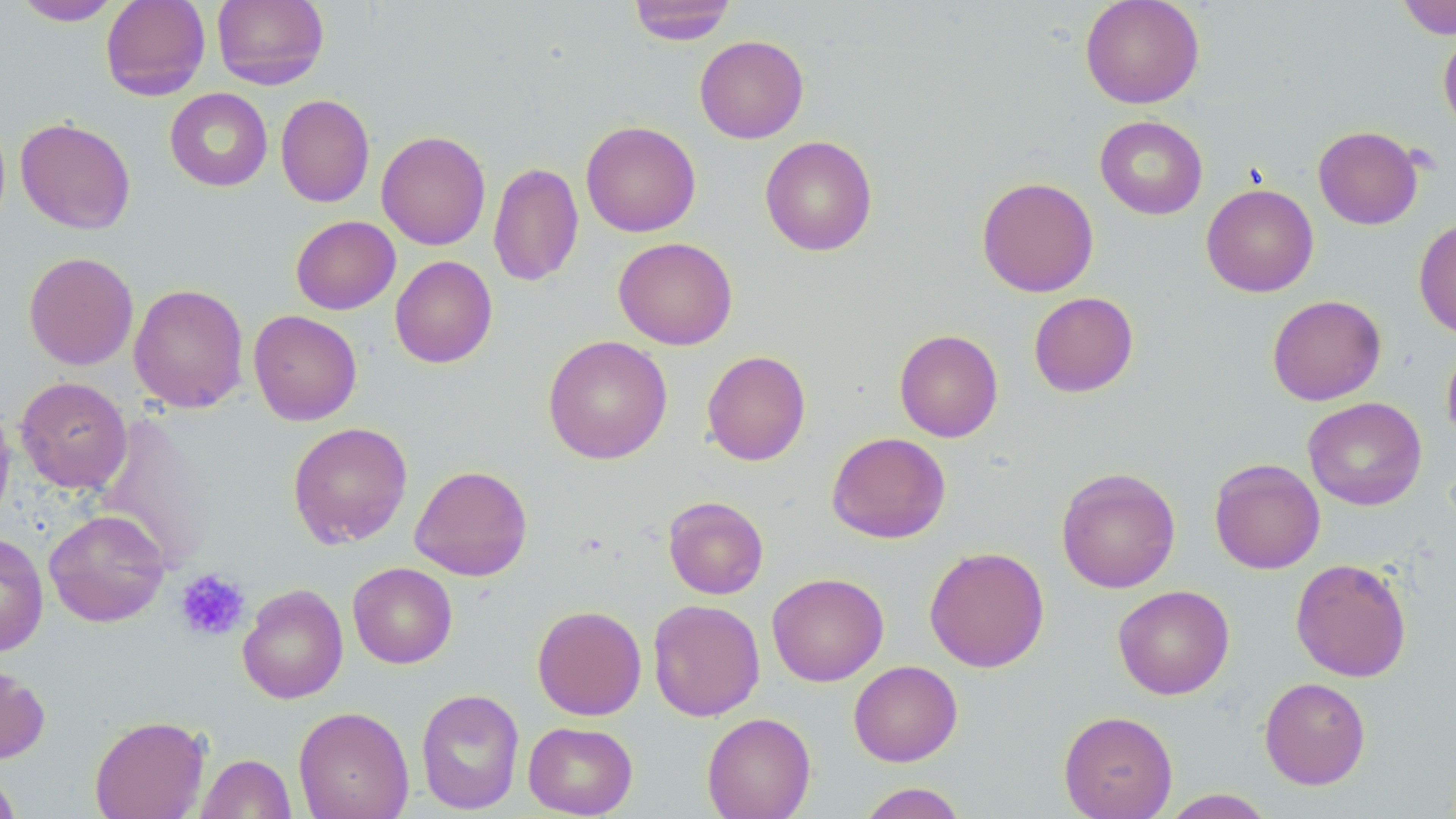
Summary:
  - Coordinate format: approximate bounding boxes as [x1, y1, x2, y2] in pixels
  - Platelet locations: [175, 568, 251, 642]
  - Uninfected red blood cell locations: [13, 0, 123, 25], [100, 0, 211, 100], [212, 0, 329, 90], [628, 0, 736, 45], [1080, 0, 1205, 109], [1396, 0, 1456, 39], [1438, 30, 1456, 134], [694, 35, 809, 143], [164, 88, 273, 191], [276, 94, 375, 208], [1095, 115, 1208, 219], [15, 117, 135, 234], [580, 120, 701, 237], [1313, 125, 1423, 230], [376, 130, 491, 250], [759, 135, 877, 256], [488, 161, 584, 287], [976, 176, 1099, 297], [1201, 183, 1319, 297], [290, 215, 400, 314], [1414, 217, 1456, 340], [613, 237, 738, 350], [23, 251, 138, 370], [390, 255, 497, 369], [129, 283, 249, 413], [1028, 292, 1139, 397], [1267, 294, 1386, 405], [248, 310, 362, 425], [894, 329, 1003, 442], [543, 335, 673, 464], [1441, 342, 1456, 448], [702, 350, 811, 466], [15, 376, 132, 494], [1303, 397, 1427, 511], [0, 398, 15, 530], [97, 411, 216, 570], [288, 421, 413, 548], [826, 431, 950, 544], [1209, 458, 1325, 574], [410, 464, 532, 581], [1056, 467, 1181, 594], [663, 496, 769, 599], [43, 509, 170, 627], [0, 533, 48, 656], [924, 546, 1050, 673], [1290, 557, 1413, 682], [347, 562, 457, 669], [766, 572, 889, 686], [237, 583, 348, 704], [1113, 585, 1235, 700], [649, 593, 887, 709], [648, 599, 765, 721], [532, 605, 647, 720], [848, 660, 963, 767], [0, 662, 50, 765], [1259, 676, 1371, 790], [416, 687, 525, 814], [293, 706, 414, 819], [1059, 710, 1178, 819], [702, 712, 816, 819], [89, 714, 210, 819], [522, 721, 638, 817], [196, 753, 296, 818], [0, 768, 21, 819], [856, 783, 968, 819], [1161, 789, 1276, 818]
  - Slide-level diagnosis: negative for blood parasites
  - Modality: optical microscopy
  - Field of view: one of a larger specimen
  - Magnification: 1000x
  - Stain: May-Grünwald-Giemsa
  - Preparation: thin blood smear
  - Image size: 1456×819 pixels